Assess the morphology of the red blood cells.
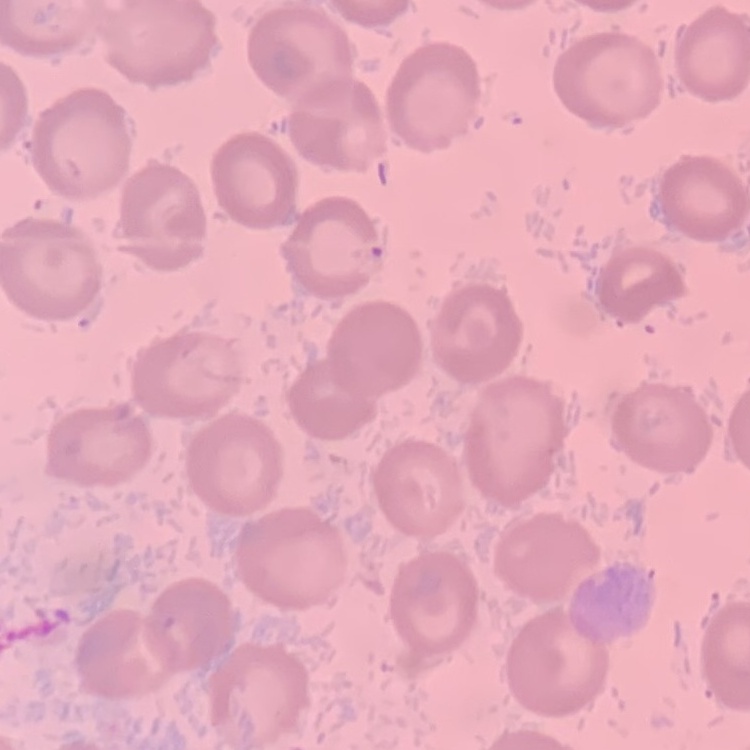

They show no rouleaux formation.

image type = square crop of a larger photomicrograph
preparation = thin blood smear
stain = Field's or Giemsa